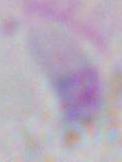

Summary:
  - Modality: micrograph
  - Identification: Toxoplasma gondii
  - Magnification: 1000x